Locate every Plasmodium falciparum parasite and identify its life-cycle stage.
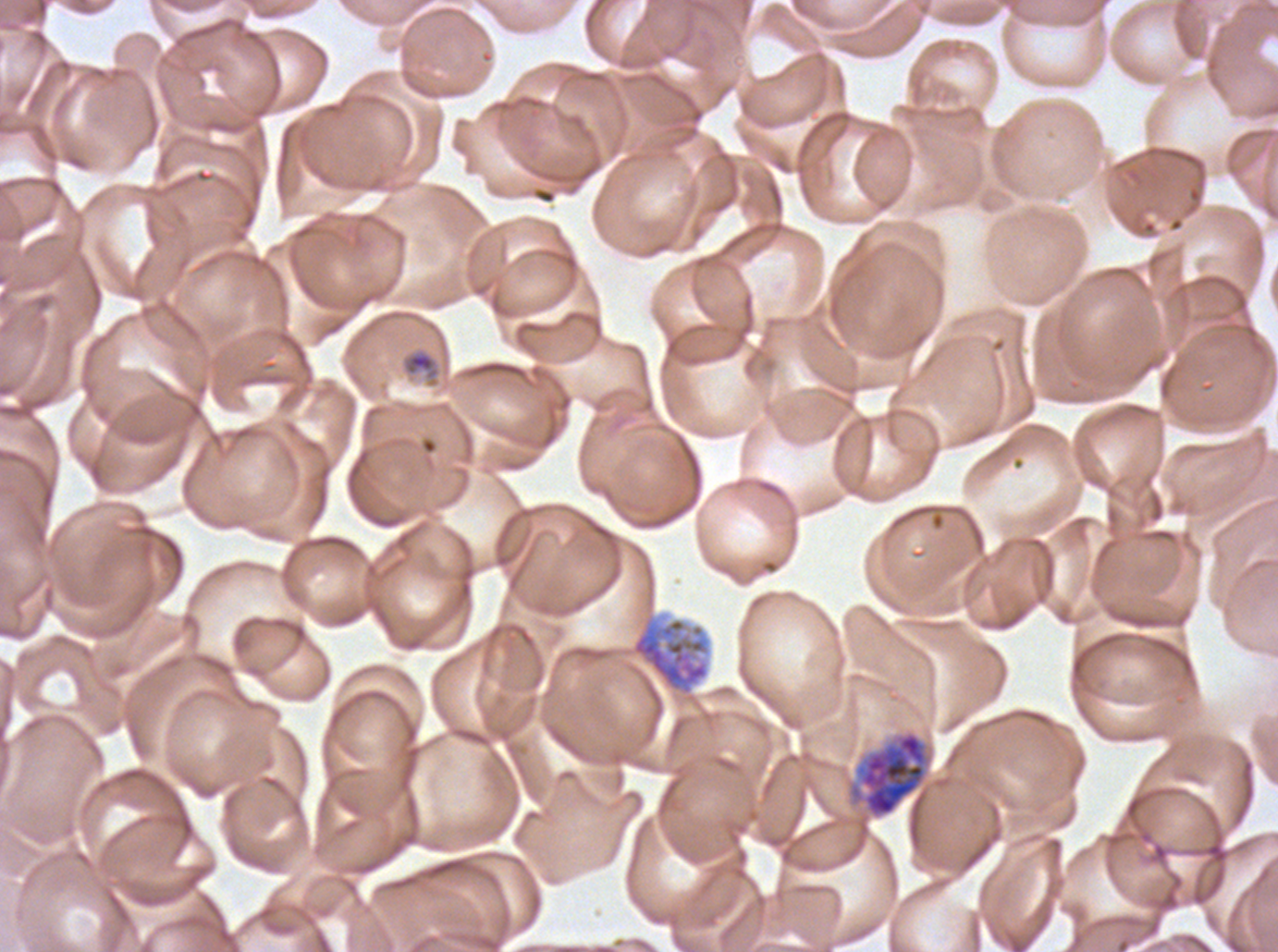

Approximate bounding boxes as [x1, y1, x2, y2] in pixels.
Late-ring/early-trophozoite forms: [401, 348, 440, 382].
Early schizonts: [849, 730, 928, 819].
Segmenters: [617, 540, 724, 735].
No rings, mid trophozoites, late trophozoites, late schizonts, or gametocytes observed.

Summary:
  - Preparation: thin blood smear
  - Field of view: one sub-image of a larger composite
  - Life-cycle stages observed: late-ring/early-trophozoite, early schizont, segmenter
  - Specimen: Plasmodium falciparum cultured ex vivo for 24 to 48 hours, from a patient in The Gambia
  - Stain: Giemsa
  - Image size: 1278×952 pixels